Report the malaria status of this cell.
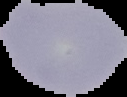

It is uninfected.

Segmented cell region on a black background. Image is 127×97 pixels. From a thin blood smear.